Point out each leukocyte.
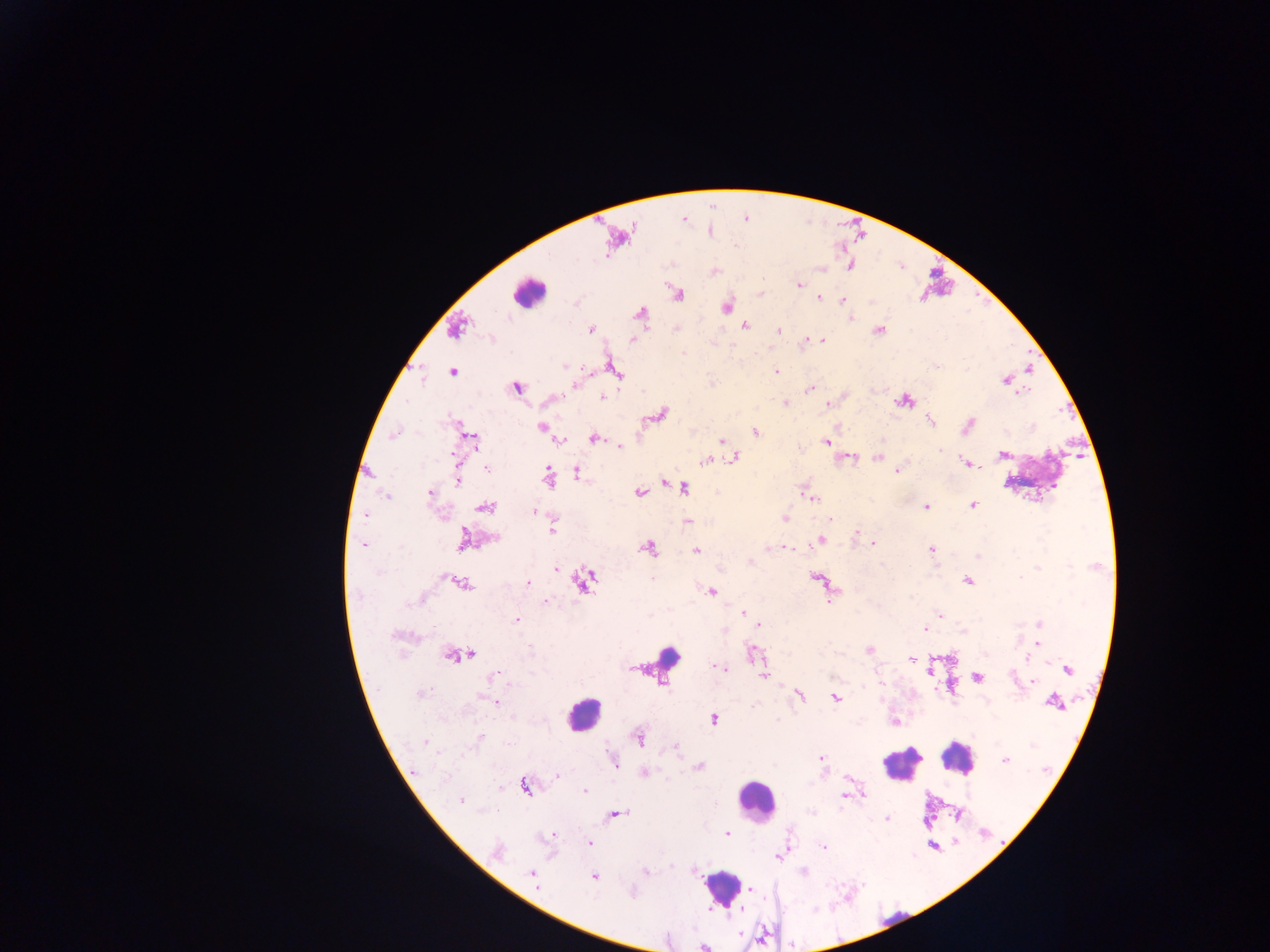
Approximate centers as x y in pixels.
Leukocytes: 528 293; 668 656; 583 713; 957 759; 900 764; 756 801; 722 888.

Plasmodium parasite locations: 799 285; 678 295; 819 298; 842 300; 726 306; 639 312; 851 318; 744 325; 878 329; 591 330; 779 330; 631 340; 821 340; 806 341; 565 365; 615 369; 1028 369; 776 371; 453 372; 1004 380; 574 384; 516 387; 810 390; 1023 392; 602 397; 785 402; 905 402; 828 404; 662 413; 930 420; 969 424; 541 427; 755 431; 393 435; 594 438; 472 439; 559 440; 721 440; 827 442; 620 446; 941 450; 1003 454; 734 457; 877 458; 705 460; 964 462; 975 464; 979 466; 486 468; 897 471; 577 472; 548 478; 457 481; 664 482; 684 487; 429 493; 639 493; 386 496; 811 498; 973 505; 485 507; 925 507; 534 511; 364 515; 784 518; 830 520; 687 521; 552 530; 856 532; 494 538; 463 539; 821 540; 873 543; 364 544; 786 547; 649 549; 931 549; 697 551; 978 556; 750 561; 936 567; 1038 567; 556 569; 1020 577; 652 578; 816 578; 967 581; 584 582; 527 583; 463 584; 711 591; 911 596; 830 601; 546 602; 742 613; 940 615; 516 619; 1039 624; 759 625; 925 628; 1038 643; 869 650; 471 654; 753 654; 449 656; 1027 659; 912 660; 719 668; 1068 670; 763 676; 493 677; 978 678; 1033 680; 510 684; 881 684; 420 694; 800 696; 835 697; 485 698; 495 702; 1053 702; 754 706; 713 719; 894 722; 479 737; 639 738; 425 742; 675 747; 821 758; 613 760; 1005 760; 699 767; 645 772; 557 775; 524 786; 584 791; 863 794; 843 797; 461 801; 617 814; 887 819; 727 833; 553 834; 589 842; 823 847; 497 850; 779 856; 804 872; 531 873; 646 873; 593 877; 751 889; 631 892; 704 947. Thick blood smear. Collected in Ghana. One field of view. Image is 1270×952 pixels. Mobile-phone photograph taken through the microscope.